Name the parasite shown.
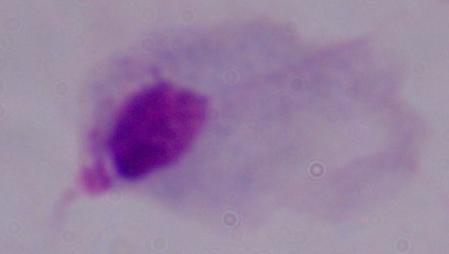

This is a trichomonad.

magnification: 1000x
modality: photomicrograph